Report the malaria status of this cell.
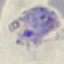
Parasitized.

image_type: automatically extracted cell patch, resized to 64 × 64 pixels
capture: smartphone through the microscope eyepiece
stain: Giemsa
preparation: thin blood film